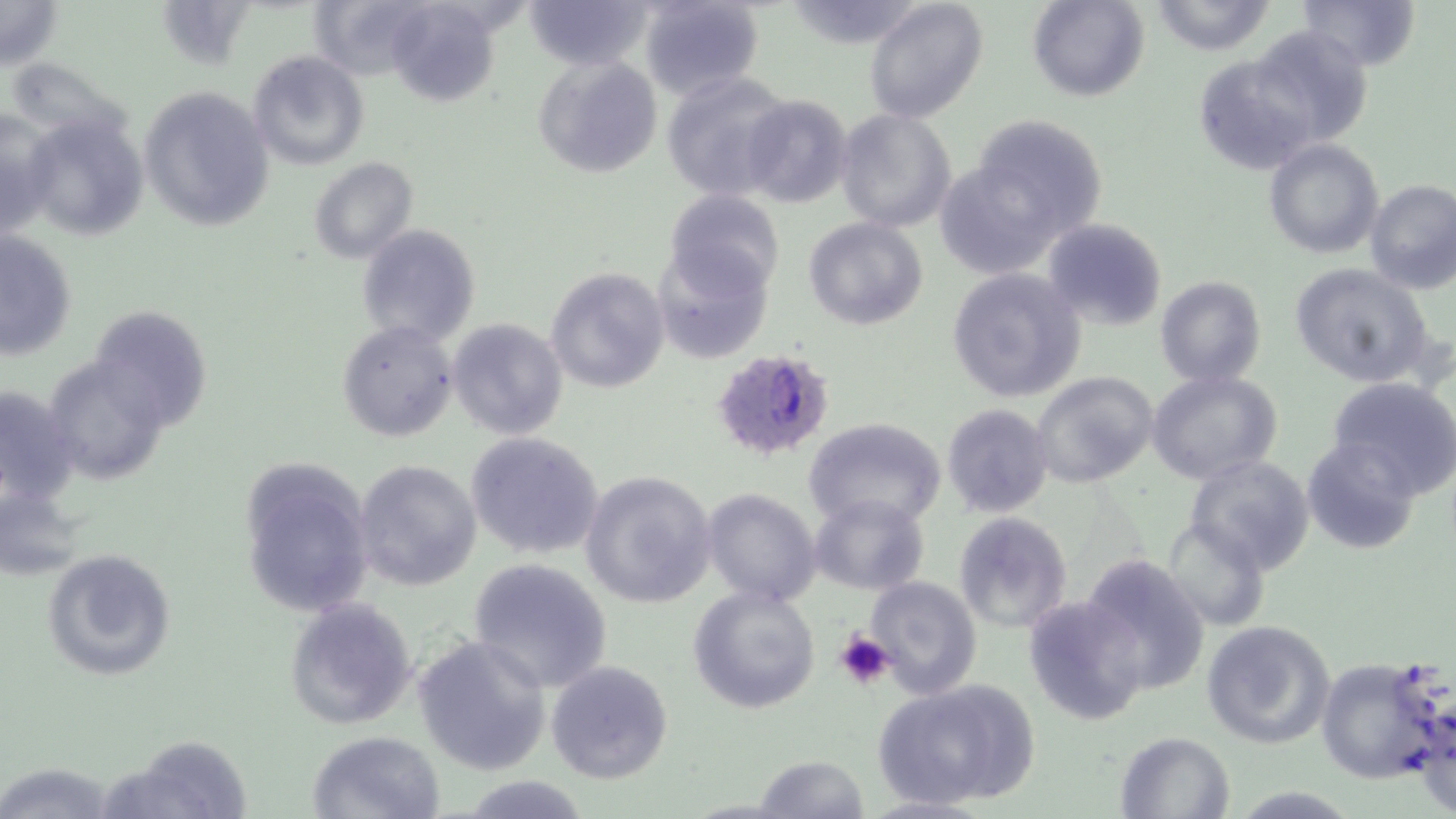

slide-level diagnosis = Plasmodium falciparum
image size = 1456×819 pixels
preparation = thin blood film
field of view = single
stain = May-Grünwald-Giemsa
uninfected red blood cell locations = approximate bounding boxes as named x1/y1/x2/y2 corners in pixels: (x1=0, y1=0, x2=65, y2=71), (x1=383, y1=0, x2=505, y2=105), (x1=639, y1=0, x2=765, y2=102), (x1=864, y1=0, x2=990, y2=125), (x1=1027, y1=0, x2=1148, y2=102), (x1=1148, y1=0, x2=1278, y2=56), (x1=1299, y1=0, x2=1420, y2=73), (x1=526, y1=1, x2=656, y2=69), (x1=783, y1=1, x2=928, y2=48), (x1=1244, y1=26, x2=1374, y2=148), (x1=247, y1=51, x2=369, y2=171), (x1=1193, y1=52, x2=1321, y2=177), (x1=533, y1=54, x2=662, y2=177), (x1=661, y1=70, x2=793, y2=200), (x1=138, y1=85, x2=274, y2=234), (x1=738, y1=94, x2=852, y2=208), (x1=0, y1=103, x2=54, y2=239), (x1=835, y1=110, x2=957, y2=234), (x1=21, y1=113, x2=150, y2=242), (x1=961, y1=116, x2=1108, y2=257), (x1=1263, y1=138, x2=1383, y2=259), (x1=933, y1=156, x2=1075, y2=280), (x1=308, y1=157, x2=419, y2=265), (x1=1364, y1=179, x2=1456, y2=294), (x1=663, y1=189, x2=787, y2=298), (x1=803, y1=217, x2=928, y2=330), (x1=1042, y1=217, x2=1168, y2=332), (x1=357, y1=222, x2=479, y2=346), (x1=0, y1=228, x2=78, y2=361), (x1=652, y1=243, x2=774, y2=363), (x1=1290, y1=264, x2=1437, y2=388), (x1=544, y1=267, x2=669, y2=393), (x1=945, y1=267, x2=1086, y2=403), (x1=1155, y1=276, x2=1266, y2=386), (x1=90, y1=306, x2=214, y2=428), (x1=446, y1=318, x2=570, y2=441), (x1=336, y1=319, x2=458, y2=443), (x1=41, y1=354, x2=169, y2=485), (x1=1148, y1=369, x2=1282, y2=486), (x1=1030, y1=371, x2=1159, y2=490), (x1=1327, y1=376, x2=1456, y2=498), (x1=0, y1=384, x2=81, y2=508), (x1=940, y1=403, x2=1054, y2=518), (x1=803, y1=417, x2=949, y2=531), (x1=465, y1=433, x2=603, y2=558), (x1=1302, y1=436, x2=1421, y2=555), (x1=1184, y1=454, x2=1316, y2=574), (x1=241, y1=455, x2=374, y2=618), (x1=354, y1=459, x2=483, y2=592), (x1=580, y1=471, x2=718, y2=610), (x1=0, y1=485, x2=87, y2=580), (x1=701, y1=488, x2=820, y2=607), (x1=808, y1=494, x2=929, y2=595), (x1=951, y1=512, x2=1071, y2=634), (x1=1161, y1=516, x2=1271, y2=634), (x1=42, y1=547, x2=177, y2=682), (x1=1078, y1=552, x2=1211, y2=698), (x1=466, y1=557, x2=614, y2=693), (x1=865, y1=577, x2=982, y2=698), (x1=688, y1=586, x2=821, y2=715), (x1=1023, y1=597, x2=1146, y2=726), (x1=284, y1=598, x2=418, y2=730), (x1=1199, y1=620, x2=1335, y2=749), (x1=412, y1=635, x2=552, y2=775), (x1=1315, y1=657, x2=1447, y2=784), (x1=546, y1=660, x2=674, y2=785), (x1=874, y1=679, x2=1033, y2=810), (x1=306, y1=730, x2=445, y2=818), (x1=1114, y1=730, x2=1238, y2=819), (x1=107, y1=735, x2=255, y2=819), (x1=752, y1=753, x2=873, y2=818), (x1=0, y1=761, x2=121, y2=817), (x1=457, y1=776, x2=596, y2=816)
Plasmodium falciparum-infected red blood cell locations = approximate bounding boxes as named x1/y1/x2/y2 corners in pixels: (x1=709, y1=349, x2=836, y2=460)
platelet locations = approximate bounding boxes as named x1/y1/x2/y2 corners in pixels: (x1=835, y1=630, x2=895, y2=691)
magnification = 1000x
modality = optical microscopy